Identify the blood parasite species.
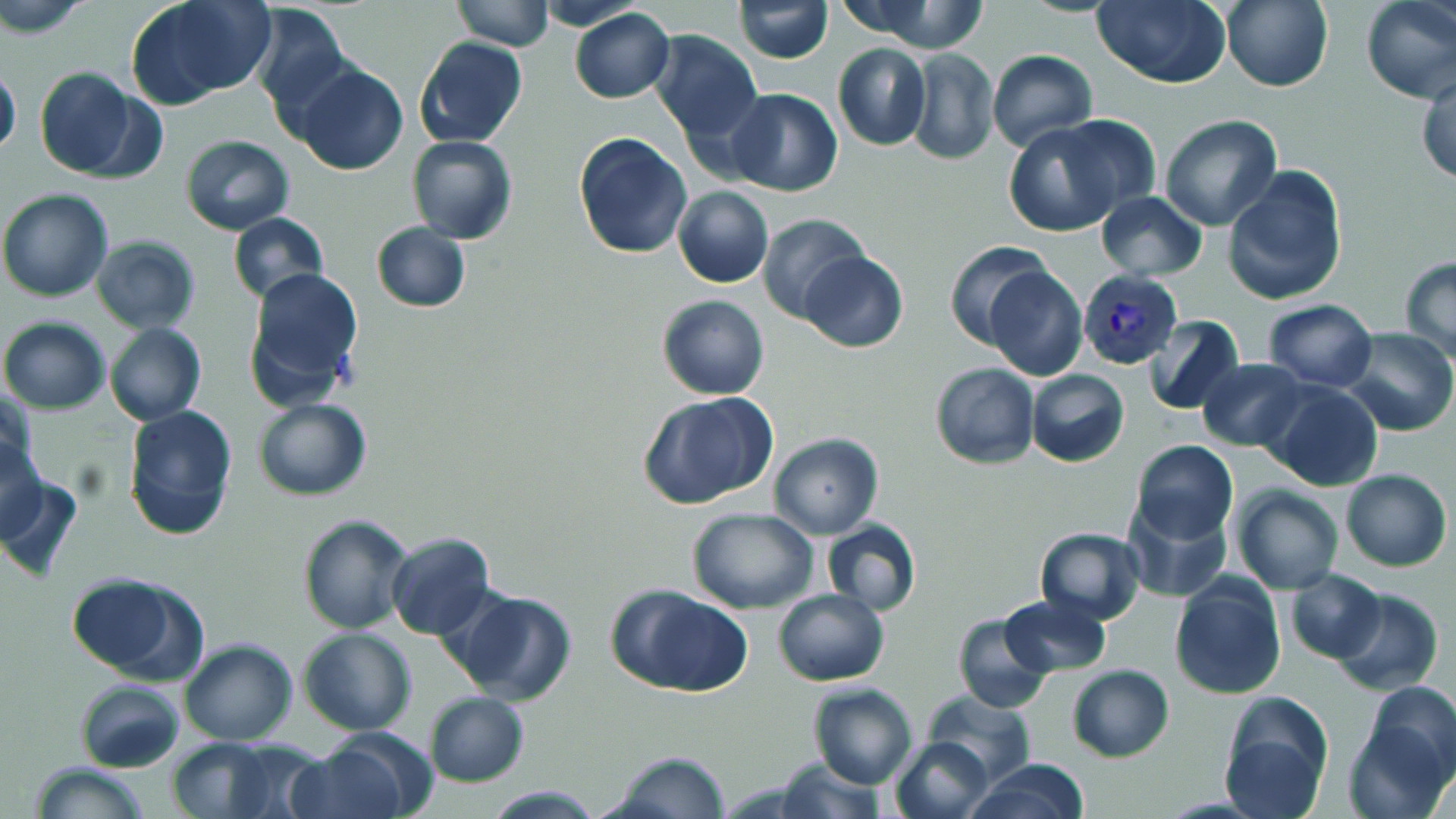

Plasmodium vivax.

Approximate bounding boxes as (x1,y1)-(x2,y2) corner pairs in pixels. Uninfected red blood cell locations: (137,0)-(274,101), (452,0)-(553,51), (534,0)-(651,30), (734,0)-(832,63), (1093,0)-(1231,89), (1223,0)-(1333,92), (1361,0)-(1455,103), (847,1)-(992,54), (0,2)-(94,40), (250,5)-(352,121), (570,7)-(674,104), (651,30)-(761,140), (413,37)-(526,149), (832,43)-(930,152), (907,48)-(998,164), (987,50)-(1096,150), (0,64)-(21,159), (295,64)-(408,177), (34,66)-(144,180), (1416,69)-(1456,186), (725,89)-(843,197), (1056,113)-(1160,217), (1160,114)-(1283,231), (1003,118)-(1134,238), (574,132)-(692,259), (180,134)-(296,236), (406,136)-(517,244), (1223,166)-(1348,306), (673,186)-(774,288), (0,188)-(113,302), (1095,191)-(1208,279), (227,213)-(329,306), (758,213)-(870,324), (371,222)-(471,311), (91,233)-(200,333), (944,239)-(1053,349), (799,250)-(907,352), (1399,255)-(1456,362), (983,265)-(1087,381), (243,267)-(365,403), (656,294)-(770,400), (1263,299)-(1378,391), (1144,315)-(1247,415), (0,317)-(112,414), (104,323)-(206,426), (1339,328)-(1455,436), (1197,359)-(1306,451), (930,362)-(1038,469), (1026,369)-(1130,466), (1262,381)-(1383,492), (1,386)-(36,481), (637,390)-(777,510), (252,397)-(372,500), (122,404)-(237,541), (768,432)-(885,539), (1,438)-(46,542), (1129,440)-(1238,546), (1340,468)-(1452,573), (2,470)-(84,584), (1234,479)-(1451,582), (1230,486)-(1344,595), (1124,502)-(1232,601), (686,508)-(818,614), (297,513)-(417,635), (821,519)-(921,617), (1034,526)-(1147,624), (385,531)-(497,641), (1283,569)-(1386,664), (64,572)-(201,681), (1170,575)-(1287,701), (610,586)-(752,697), (447,588)-(577,705), (773,588)-(890,686), (1331,588)-(1443,696), (1001,593)-(1112,677), (951,611)-(1056,714), (299,626)-(416,735), (180,640)-(298,745), (1066,665)-(1175,762), (75,679)-(186,772), (807,682)-(917,789), (1365,682)-(1456,780), (923,691)-(1035,785), (424,692)-(529,788), (1217,694)-(1334,817), (1342,717)-(1452,819), (891,737)-(994,819), (168,738)-(275,818), (224,739)-(330,817), (288,740)-(412,819), (607,751)-(731,819), (771,756)-(885,819), (965,759)-(1090,818), (28,761)-(149,819), (481,786)-(607,817). Plasmodium vivax-infected red blood cell locations: (1080,269)-(1181,369). Optical microscopy. Single field of view. May-Grünwald-Giemsa stain. Captured at 1000x magnification. Image is 1456×819 pixels. Thin blood smear.